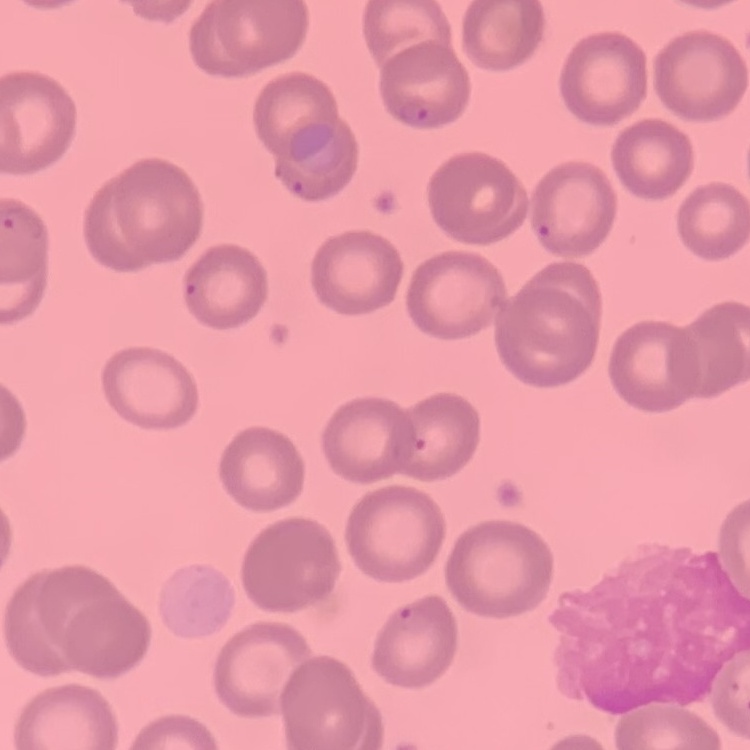

Summary:
  - Erythrocyte morphology: no rouleaux formation
  - Stain: Field's or Giemsa
  - Preparation: thin peripheral smear
  - Image type: one tile cut from a larger photomicrograph